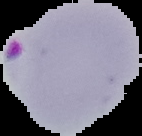
{
  "image_type": "segmented cell region with the area outside set to black",
  "preparation": "thin blood smear",
  "malaria_status": "parasitized",
  "image_size": "142×136 pixels"
}